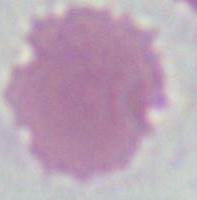
Photomicrograph. 1000x magnification. A red blood cell is seen.